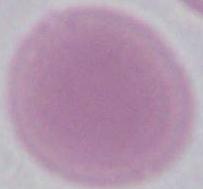
identification = red blood cell
modality = micrograph
magnification = 1000x